State which parasite is depicted.
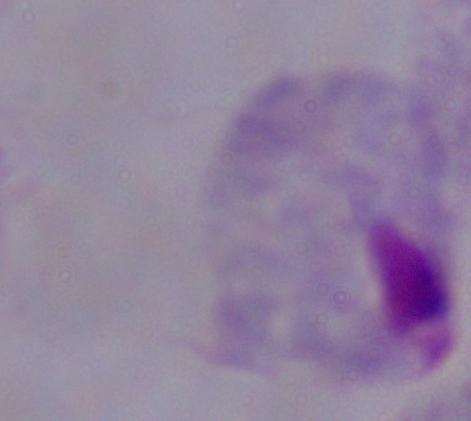

This is a trichomonad.

{
  "magnification": "1000x",
  "modality": "photomicrograph"
}